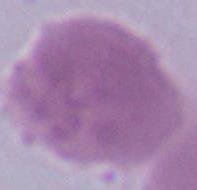
Summary:
  - Modality: photomicrograph
  - Identification: erythrocyte
  - Magnification: 1000x